Identify the blood parasite species.
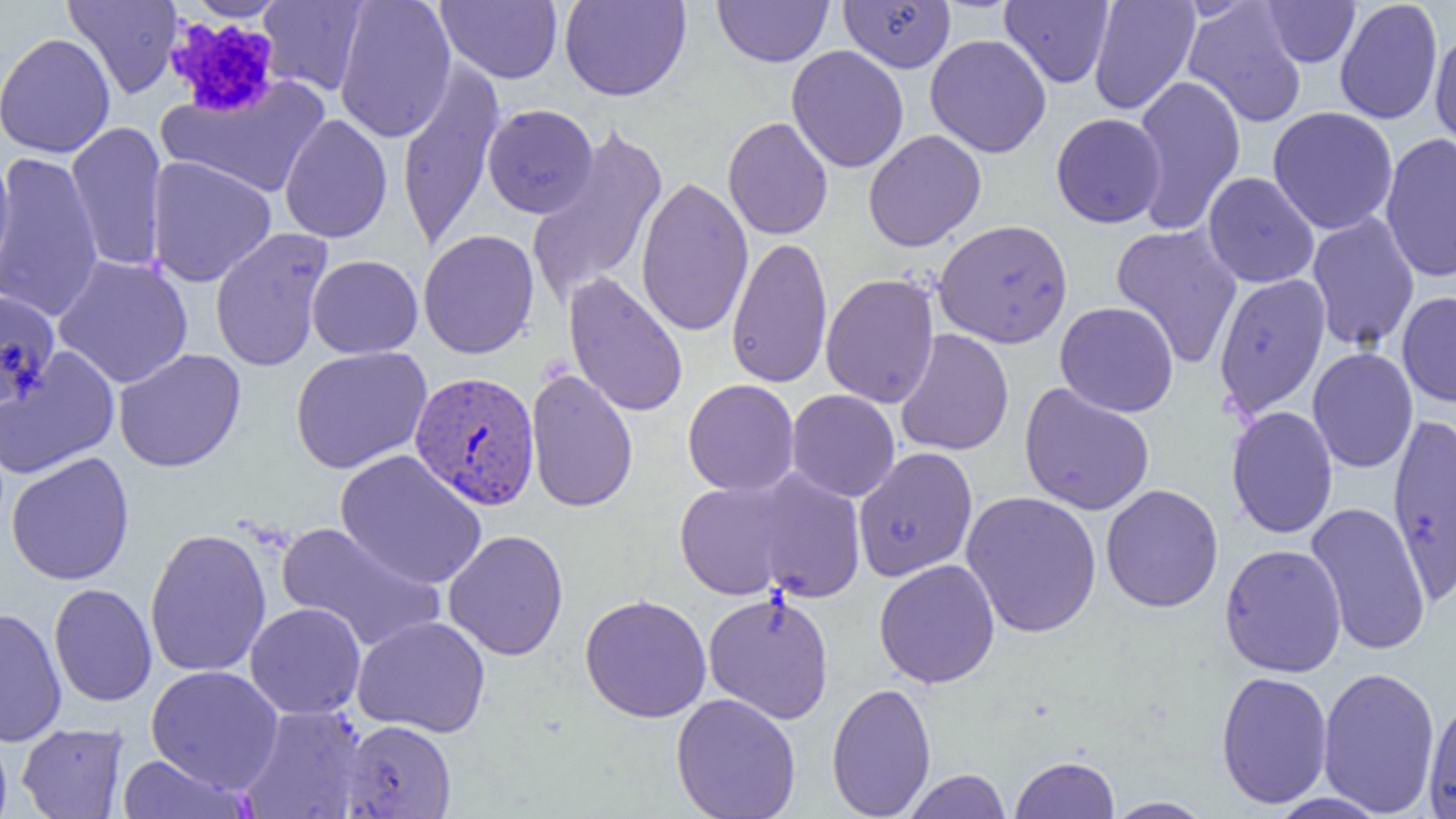

Plasmodium vivax.

Approximate bounding boxes as named x1/y1/x2/y2 corners in pixels. Uninfected red blood cell locations: (x1=63, y1=0, x2=183, y2=99), (x1=186, y1=0, x2=289, y2=21), (x1=334, y1=0, x2=457, y2=143), (x1=436, y1=0, x2=562, y2=83), (x1=559, y1=0, x2=691, y2=101), (x1=713, y1=0, x2=833, y2=67), (x1=839, y1=0, x2=956, y2=73), (x1=1000, y1=0, x2=1114, y2=88), (x1=1088, y1=0, x2=1200, y2=115), (x1=1335, y1=0, x2=1443, y2=125), (x1=258, y1=1, x2=369, y2=95), (x1=1261, y1=1, x2=1361, y2=67), (x1=1183, y1=2, x2=1307, y2=128), (x1=1430, y1=27, x2=1456, y2=154), (x1=0, y1=32, x2=115, y2=158), (x1=925, y1=34, x2=1052, y2=158), (x1=786, y1=45, x2=909, y2=173), (x1=396, y1=60, x2=506, y2=253), (x1=1131, y1=75, x2=1247, y2=236), (x1=159, y1=76, x2=331, y2=198), (x1=482, y1=103, x2=598, y2=218), (x1=1267, y1=106, x2=1399, y2=235), (x1=279, y1=113, x2=393, y2=244), (x1=1051, y1=113, x2=1166, y2=228), (x1=722, y1=117, x2=833, y2=240), (x1=66, y1=121, x2=168, y2=273), (x1=525, y1=125, x2=669, y2=307), (x1=863, y1=129, x2=987, y2=252), (x1=1379, y1=132, x2=1456, y2=282), (x1=0, y1=151, x2=103, y2=324), (x1=0, y1=152, x2=15, y2=287), (x1=146, y1=156, x2=277, y2=287), (x1=1203, y1=172, x2=1319, y2=288), (x1=635, y1=178, x2=754, y2=337), (x1=1306, y1=212, x2=1420, y2=352), (x1=933, y1=219, x2=1073, y2=348), (x1=1110, y1=223, x2=1244, y2=369), (x1=209, y1=227, x2=333, y2=372), (x1=418, y1=229, x2=540, y2=359), (x1=726, y1=235, x2=833, y2=390), (x1=307, y1=254, x2=423, y2=358), (x1=53, y1=255, x2=194, y2=389), (x1=564, y1=271, x2=688, y2=418), (x1=821, y1=272, x2=940, y2=409), (x1=1214, y1=273, x2=1331, y2=419), (x1=0, y1=290, x2=60, y2=409), (x1=1397, y1=291, x2=1456, y2=408), (x1=1055, y1=301, x2=1179, y2=417), (x1=895, y1=328, x2=1014, y2=456), (x1=290, y1=346, x2=433, y2=474), (x1=0, y1=347, x2=120, y2=480), (x1=1307, y1=347, x2=1419, y2=473), (x1=113, y1=348, x2=246, y2=472), (x1=525, y1=369, x2=639, y2=513), (x1=682, y1=379, x2=800, y2=497), (x1=1019, y1=383, x2=1156, y2=516), (x1=786, y1=389, x2=901, y2=502), (x1=1226, y1=406, x2=1338, y2=539), (x1=1387, y1=409, x2=1456, y2=607), (x1=852, y1=447, x2=978, y2=582), (x1=335, y1=449, x2=488, y2=590), (x1=6, y1=451, x2=134, y2=585), (x1=746, y1=469, x2=866, y2=603), (x1=675, y1=478, x2=802, y2=601), (x1=1101, y1=484, x2=1224, y2=612), (x1=961, y1=490, x2=1102, y2=639), (x1=1306, y1=502, x2=1431, y2=656), (x1=276, y1=521, x2=445, y2=654), (x1=144, y1=526, x2=272, y2=679), (x1=443, y1=530, x2=569, y2=660), (x1=1219, y1=543, x2=1347, y2=677), (x1=874, y1=559, x2=1000, y2=688), (x1=49, y1=583, x2=157, y2=707), (x1=703, y1=590, x2=835, y2=724), (x1=579, y1=594, x2=712, y2=723), (x1=245, y1=602, x2=367, y2=719), (x1=0, y1=606, x2=67, y2=746), (x1=352, y1=615, x2=490, y2=738), (x1=146, y1=665, x2=284, y2=792), (x1=1318, y1=665, x2=1441, y2=817), (x1=1216, y1=671, x2=1334, y2=809), (x1=827, y1=681, x2=936, y2=818), (x1=671, y1=693, x2=801, y2=819), (x1=1424, y1=696, x2=1456, y2=819), (x1=237, y1=705, x2=367, y2=819), (x1=340, y1=720, x2=457, y2=818), (x1=17, y1=723, x2=129, y2=818), (x1=0, y1=726, x2=12, y2=819), (x1=117, y1=754, x2=252, y2=818), (x1=1009, y1=755, x2=1120, y2=818), (x1=903, y1=769, x2=1012, y2=819), (x1=1264, y1=792, x2=1393, y2=819), (x1=1103, y1=796, x2=1215, y2=818). Platelet locations: (x1=164, y1=15, x2=282, y2=119). Plasmodium vivax-infected red blood cell locations: (x1=410, y1=371, x2=540, y2=510). Captured at 1000x magnification. Light microscopy. Thin blood film. Single field of view. Image is 1456×819 pixels.